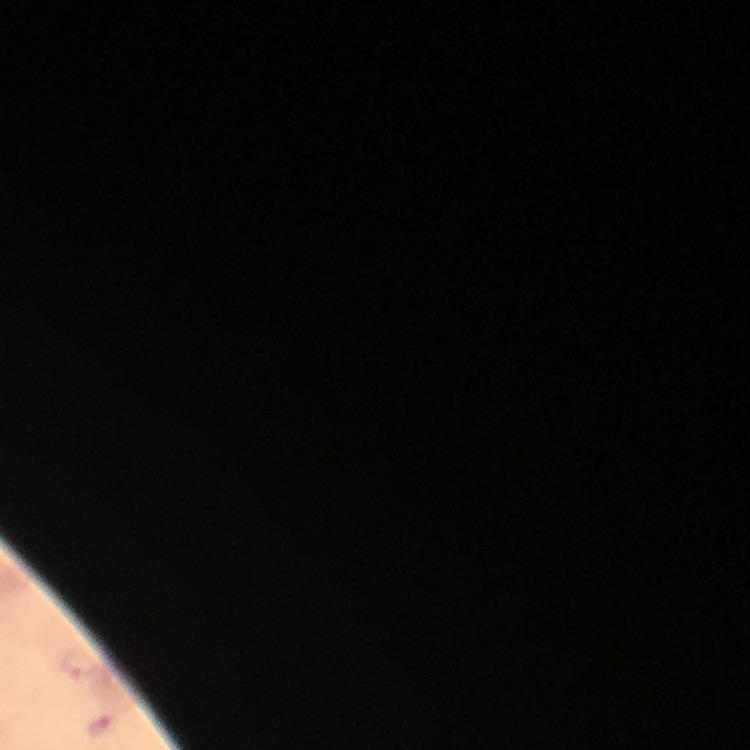

Approximate centers as [x, y] in pixels. Plasmodium parasite locations: [77, 665], [101, 727]. Immersion oil was used. From a diagnostic examination for malaria. Thick blood smear. Giemsa stain. Image is 750×750 pixels. A crop from one field of view. At 100x magnification. Photographed through the microscope with a smartphone camera.